Assess this cell for malaria.
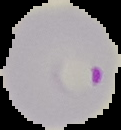

It is parasitized.

Summary:
  - Image size: 121×130 pixels
  - Image type: segmented cell region with the area outside set to black
  - Preparation: thin blood smear